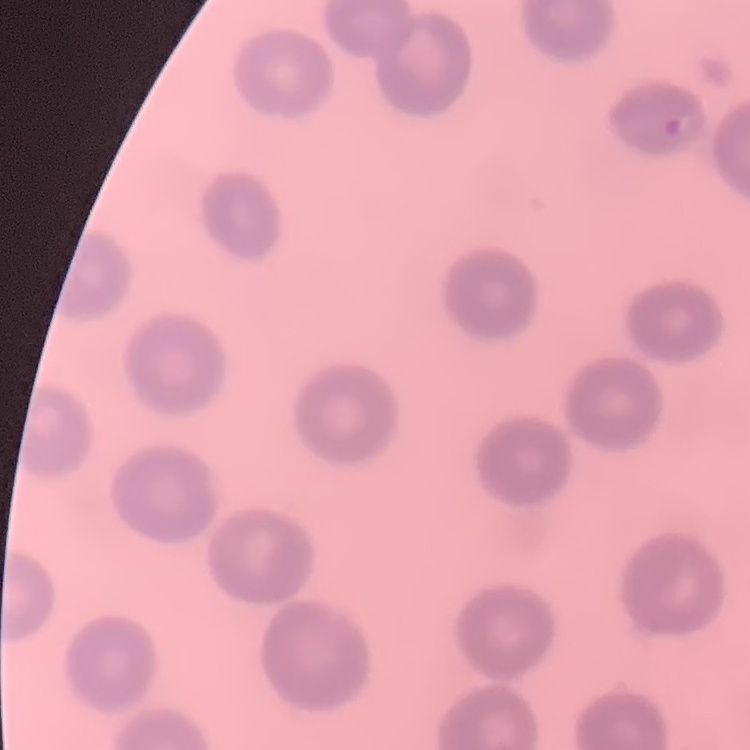 The red blood cells show no rouleaux formation. Field's or Giemsa stain. Thin blood film. One tile cut from a larger photomicrograph.